State the preparation type.
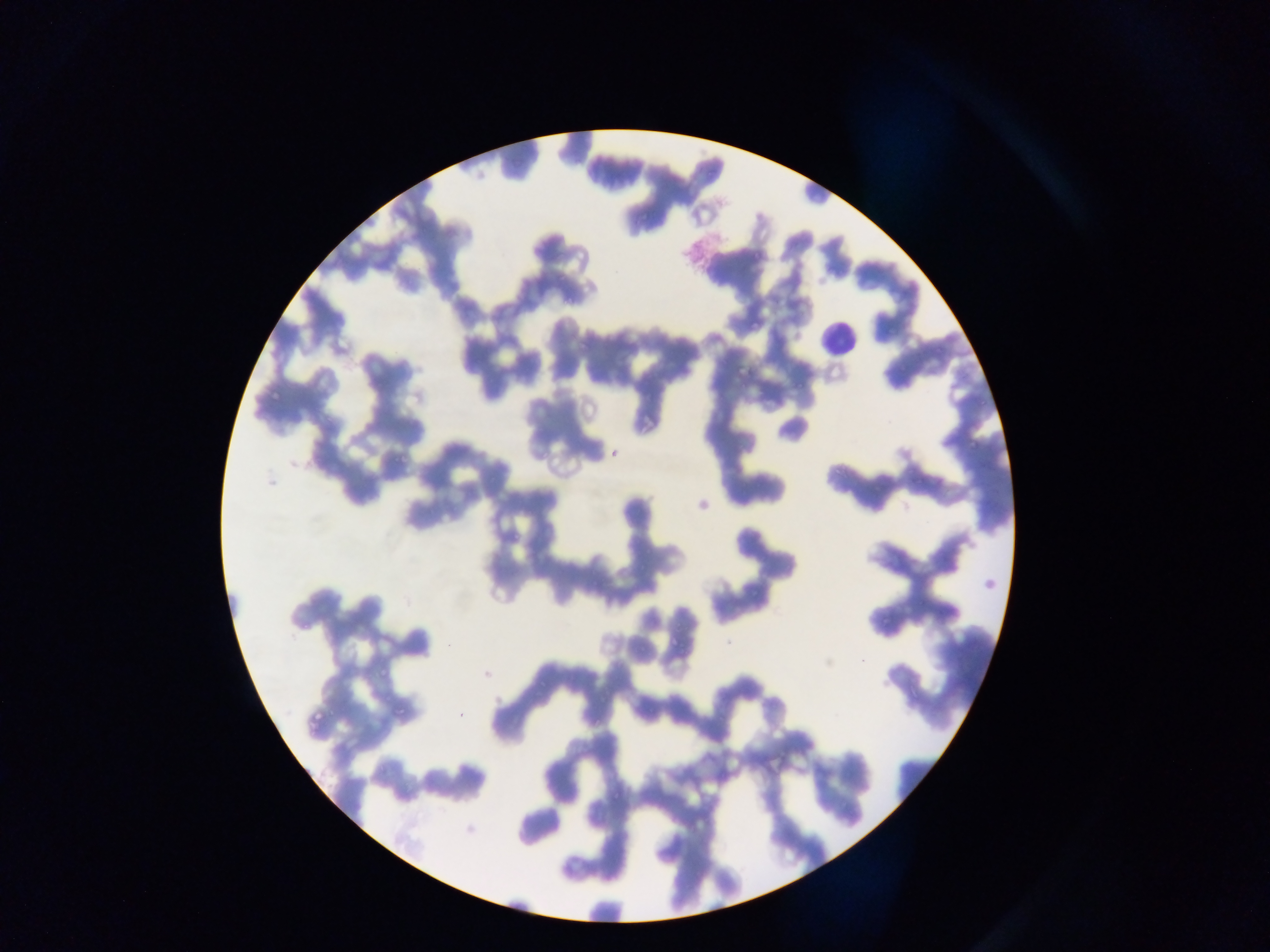

This is a thin smear.

image size = 1270×952 pixels
leukocyte locations = approximate bounding boxes as (left, top, right, bottom) in pixels: (812, 321, 861, 368)
capture = mobile-phone photograph through a microscope
country = Ghana
field of view = single